Comment on the morphology of the red blood cells.
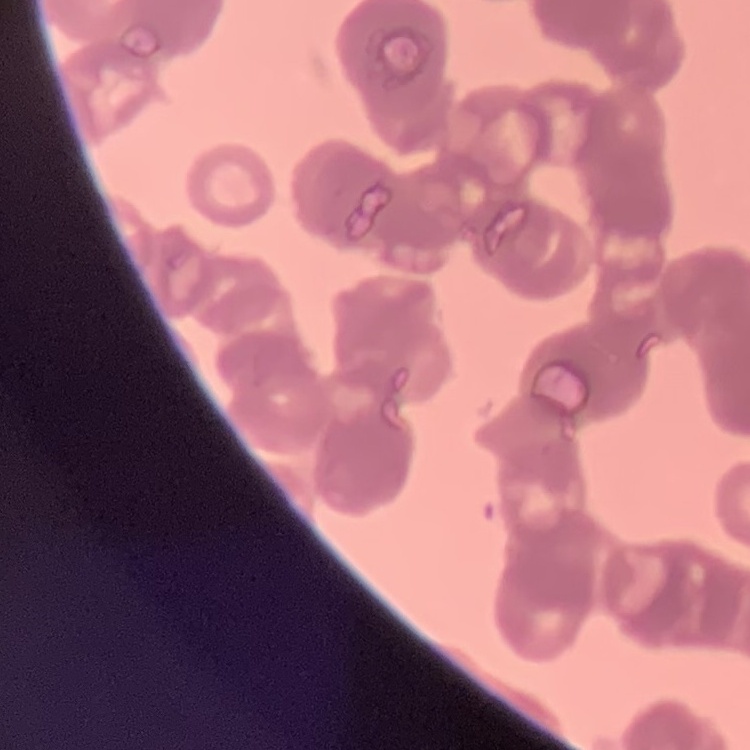

They show rouleaux formation.

Summary:
  - Image type: one tile cut from a larger photomicrograph
  - Stain: Field's or Giemsa
  - Preparation: thin blood film